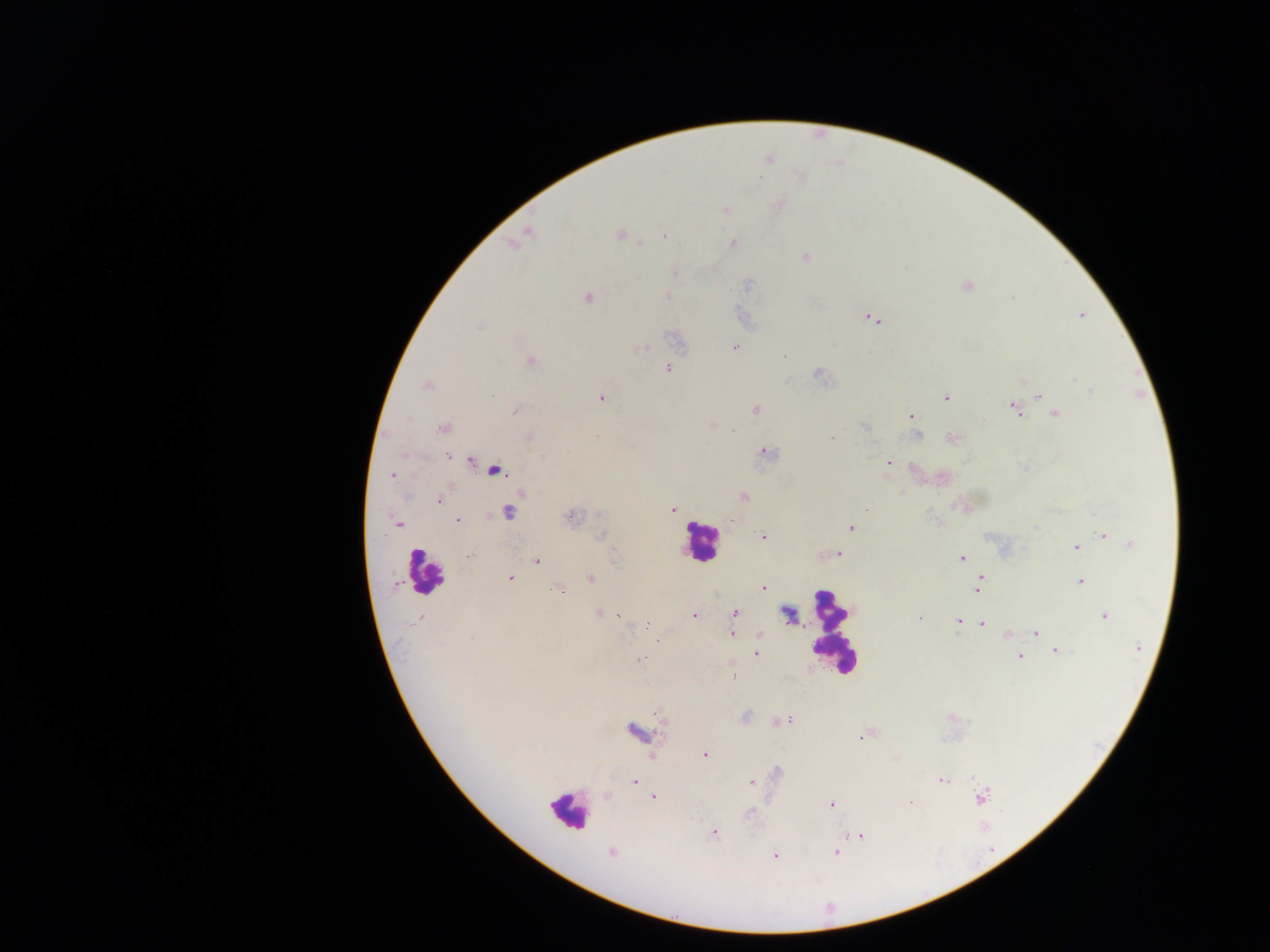

Approximate centers as {x, y} in pixels.
Summary:
  - Leukocyte locations: {700, 543}, {425, 571}, {833, 631}, {568, 810}
  - Malaria parasite locations: {726, 209}, {528, 232}, {620, 235}, {664, 237}, {732, 243}, {805, 257}, {675, 271}, {967, 286}, {667, 296}, {588, 298}, {1082, 315}, {872, 318}, {477, 325}, {674, 339}, {735, 347}, {642, 348}, {784, 356}, {530, 360}, {668, 368}, {819, 375}, {426, 385}, {1091, 391}, {491, 395}, {1039, 395}, {946, 397}, {601, 398}, {1014, 408}, {756, 409}, {515, 410}, {1055, 414}, {910, 416}, {865, 426}, {913, 426}, {443, 427}, {917, 435}, {528, 436}, {831, 437}, {953, 439}, {767, 452}, {448, 456}, {542, 457}, {471, 461}, {888, 462}, {497, 470}, {392, 475}, {742, 496}, {439, 500}, {673, 509}, {866, 509}, {508, 511}, {570, 516}, {731, 520}, {396, 522}, {458, 522}, {852, 528}, {1103, 535}, {602, 536}, {763, 536}, {1132, 544}, {1076, 547}, {838, 553}, {471, 555}, {961, 558}, {538, 561}, {509, 578}, {591, 578}, {981, 579}, {1081, 581}, {395, 584}, {762, 586}, {979, 586}, {559, 589}, {735, 612}, {598, 613}, {619, 615}, {693, 616}, {1104, 616}, {420, 618}, {920, 618}, {957, 620}, {647, 623}, {982, 624}, {1035, 632}, {732, 634}, {1006, 634}, {759, 636}, {1138, 647}, {1056, 651}, {756, 652}, {1019, 657}, {639, 658}, {733, 675}, {746, 717}, {786, 720}, {779, 721}, {635, 731}, {860, 738}, {704, 754}, {777, 772}, {974, 777}, {942, 780}, {635, 782}, {751, 783}, {654, 797}, {982, 798}, {911, 802}, {832, 805}, {750, 813}, {713, 833}, {859, 835}, {611, 853}, {836, 853}, {776, 855}
  - Image size: 1270×952 pixels
  - Field of view: single
  - Capture: mobile-phone photograph through a microscope
  - Country: Ghana
  - Preparation: thick blood film